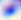
Summary:
  - Magnification: 400x
  - Modality: photomicrograph
  - Identification: Toxoplasma gondii